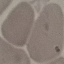
malaria status = uninfected
stain = Giemsa
image type = automatically extracted cell patch, resized to 64 × 64 pixels
capture = smartphone through the microscope eyepiece
preparation = thin blood film